Mark where platelets are.
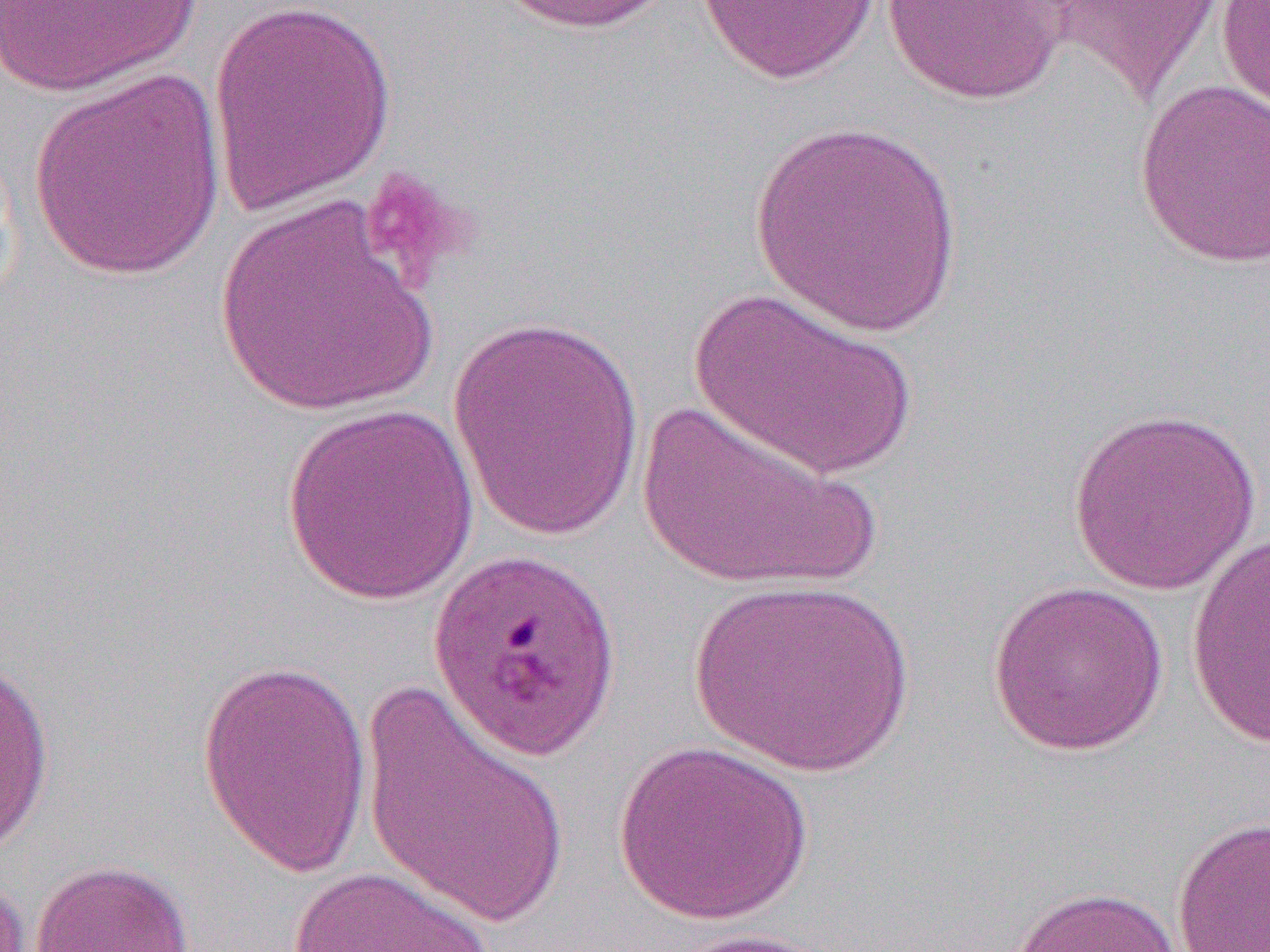

Approximate bounding boxes as (x1,y1)-(x2,y2) corner pairs in pixels.
Platelets: (357,166)-(479,289).

slide-level diagnosis = Plasmodium falciparum
field of view = one of a larger specimen
preparation = thin blood film
uninfected red blood cell locations = approximate bounding boxes as (x1,y1)-(x2,y2) corner pairs in pixels: (0,0)-(207,97), (207,0)-(397,218), (495,0)-(682,35), (694,0)-(882,85), (1049,0)-(1228,104), (1215,0)-(1270,118), (880,1)-(1069,105), (28,68)-(227,282), (1134,78)-(1270,269), (747,120)-(968,338), (215,194)-(438,418), (690,287)-(917,480), (447,314)-(649,543), (633,399)-(881,593), (279,401)-(480,607), (1067,405)-(1262,596), (1185,530)-(1270,752), (687,576)-(917,776), (986,579)-(1171,757), (1,654)-(56,863), (196,656)-(374,881), (360,680)-(573,929), (612,738)-(814,927), (1171,816)-(1270,952), (28,858)-(195,952), (286,865)-(497,952), (0,869)-(31,952), (1004,885)-(1183,952), (657,928)-(851,951)
magnification = 1000x
modality = light microscopy
image size = 1270×952 pixels